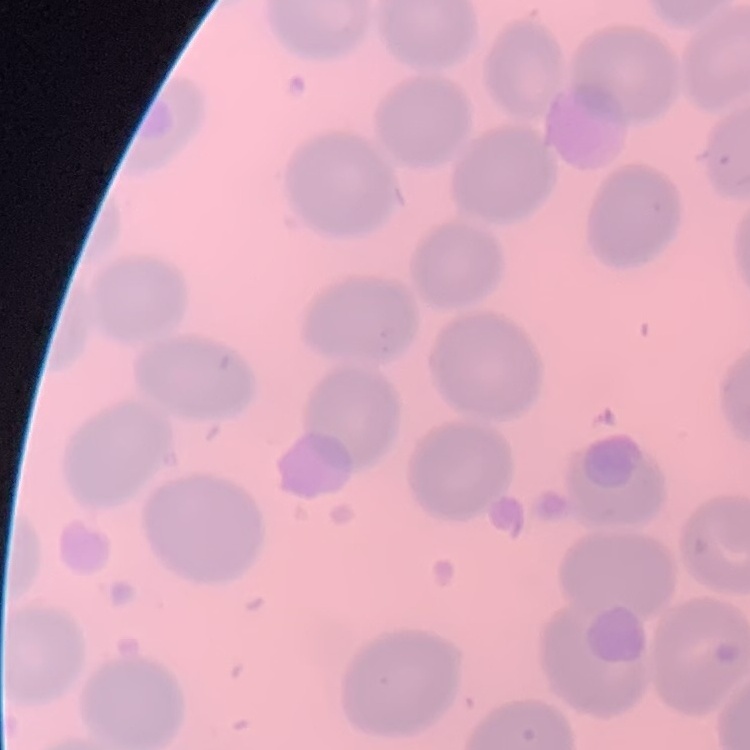

The red blood cells show no rouleaux formation. One tile cut from a larger photomicrograph. Thin blood smear. Field's or Giemsa stain.